Identify the parasite.
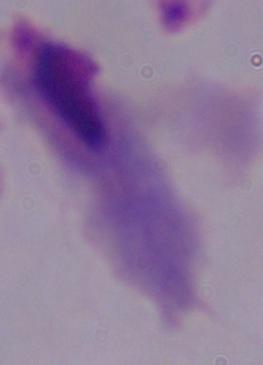
A trichomonad.

Captured at 1000x magnification. Micrograph.